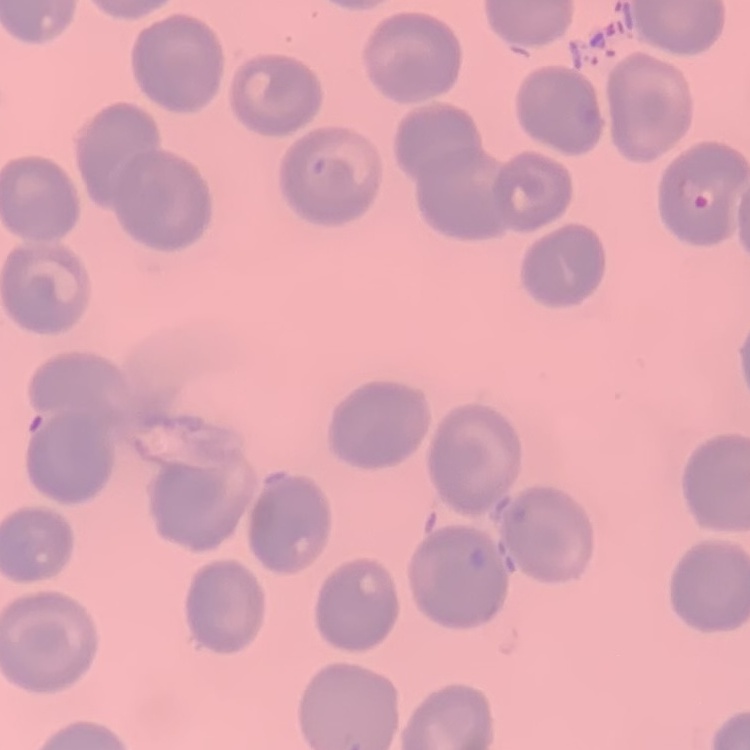 The erythrocytes exhibit no rouleaux formation. Field's or Giemsa stain. Thin blood film. Square crop of a larger photomicrograph.